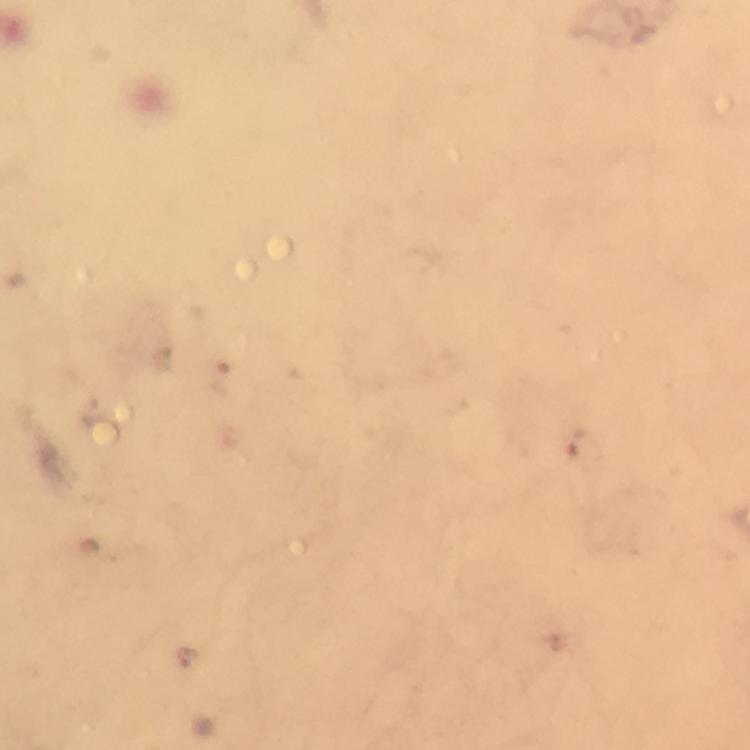
capture = smartphone camera through the microscope
Plasmodium parasite locations = approximate centers as {x, y} in pixels: {186, 656}
context = from a diagnostic examination for malaria
immersion oil = used
preparation = thick blood smear
cropped from = one field of view
magnification = 100x
stain = Giemsa
image size = 750×750 pixels